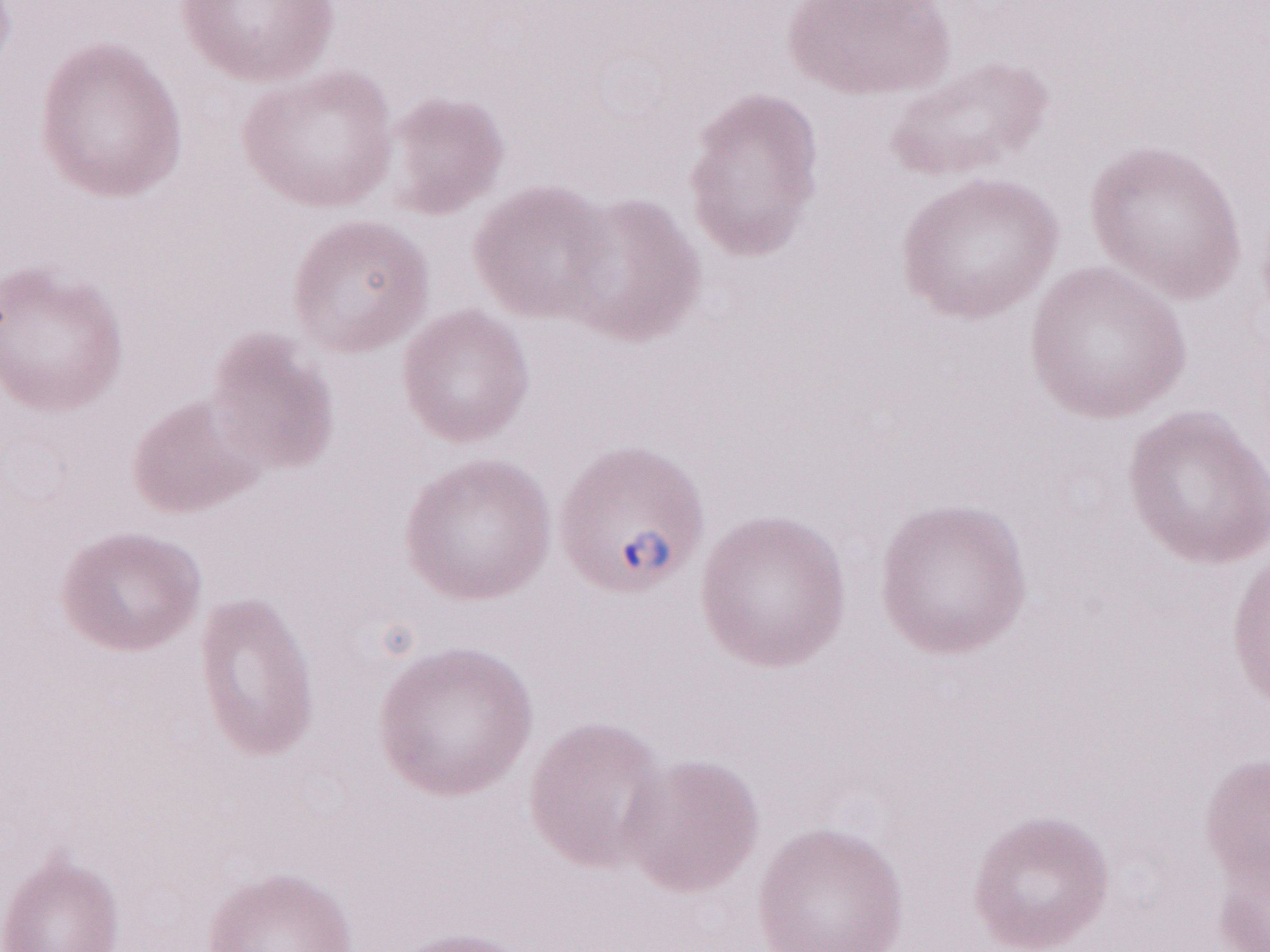

Thin blood smear. Magnification: 1,000x. One field of this slide. Olympus BX43 microscope, Olympus DP73 camera. Patient-level malaria diagnosis: positive. May-Grünwald-Giemsa (MGG) stain. Image is 1270×952 pixels.